State the blood parasite species.
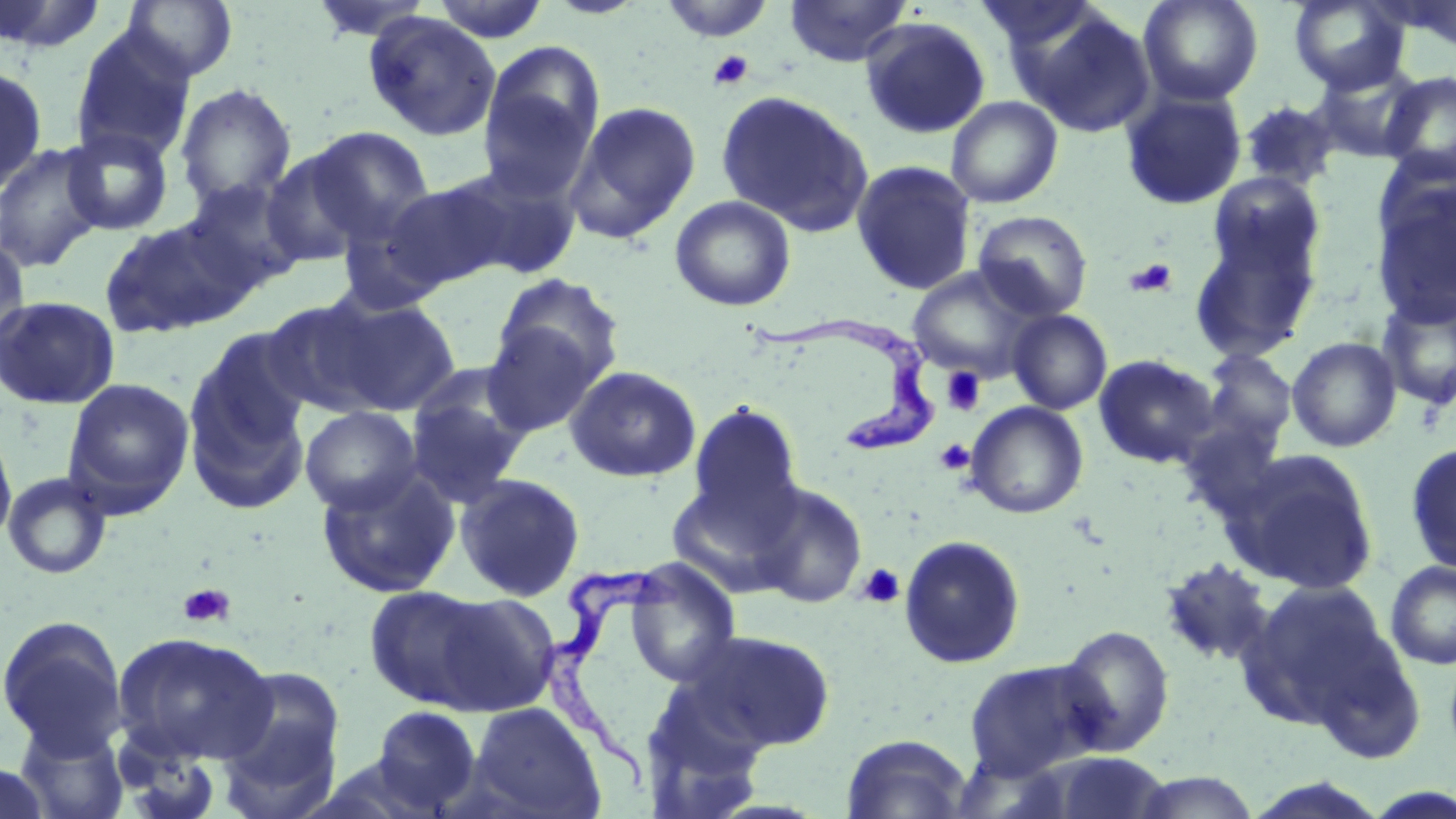

Trypanosoma brucei.

modality = optical microscopy
Trypanosoma brucei locations = approximate bounding boxes as [x1, y1, x2, y2] in pixels: [751, 316, 941, 453], [540, 561, 688, 799]
preparation = thin blood film
image size = 1456×819 pixels
magnification = 1000x
stain = May-Grünwald-Giemsa
platelet locations = approximate bounding boxes as [x1, y1, x2, y2] in pixels: [708, 49, 754, 91], [1125, 258, 1179, 298], [941, 367, 986, 415], [934, 439, 975, 475], [857, 563, 906, 608], [178, 583, 235, 628]
field of view = one of a larger specimen
uninfected red blood cell locations = approximate bounding boxes as [x1, y1, x2, y2] in pixels: [0, 0, 109, 54], [123, 0, 238, 81], [309, 0, 437, 42], [429, 0, 552, 42], [783, 0, 912, 67], [972, 0, 1109, 65], [1138, 0, 1263, 106], [1288, 0, 1411, 94], [658, 1, 778, 43], [1387, 1, 1456, 52], [1022, 9, 1156, 138], [363, 11, 502, 142], [858, 16, 991, 139], [71, 29, 196, 164], [478, 40, 605, 200], [1311, 62, 1426, 163], [0, 64, 48, 194], [1380, 71, 1456, 182], [175, 84, 296, 212], [715, 89, 873, 235], [1120, 89, 1247, 210], [946, 96, 1063, 208], [1239, 100, 1339, 190], [565, 101, 702, 243], [304, 126, 436, 242], [61, 127, 175, 236], [0, 142, 106, 274], [260, 151, 369, 267], [851, 160, 977, 295], [446, 162, 584, 279], [1208, 173, 1324, 277], [180, 176, 306, 295], [382, 178, 514, 290], [1370, 180, 1456, 328], [669, 195, 796, 312], [336, 210, 449, 316], [972, 210, 1094, 321], [98, 215, 253, 339], [1189, 222, 1322, 362], [0, 234, 30, 354], [907, 266, 1043, 382], [492, 273, 624, 387], [1376, 293, 1456, 412], [318, 294, 462, 417], [0, 295, 120, 410], [260, 296, 392, 417], [1008, 309, 1112, 415], [481, 324, 603, 437], [184, 328, 315, 507], [1287, 336, 1402, 452], [1198, 349, 1298, 450], [1093, 354, 1219, 469], [565, 365, 702, 483], [404, 375, 532, 507], [62, 377, 195, 518], [687, 401, 803, 527], [965, 402, 1088, 519], [300, 405, 422, 514], [1176, 418, 1288, 526], [0, 420, 17, 551], [1404, 441, 1456, 575], [1224, 448, 1378, 594], [316, 467, 460, 599], [3, 472, 112, 580], [454, 473, 586, 602], [665, 474, 802, 596], [750, 482, 867, 608], [898, 535, 1026, 669], [1159, 557, 1276, 668], [623, 559, 742, 688], [1385, 561, 1456, 670], [1237, 578, 1398, 730], [364, 585, 502, 711], [426, 591, 561, 716], [0, 616, 127, 753], [1056, 624, 1175, 757], [690, 629, 836, 752], [111, 631, 279, 766], [963, 659, 1104, 782], [213, 664, 348, 816], [467, 702, 605, 819], [367, 706, 485, 816], [14, 719, 129, 818], [841, 733, 973, 818], [1048, 752, 1172, 818], [1, 761, 53, 819], [1131, 769, 1258, 817]